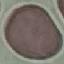

malaria_status: uninfected
stain: Giemsa
preparation: thin blood film
image_type: cell patch, automatically extracted from a larger field of view and resized to 64 × 64 pixels
capture: smartphone through the microscope eyepiece